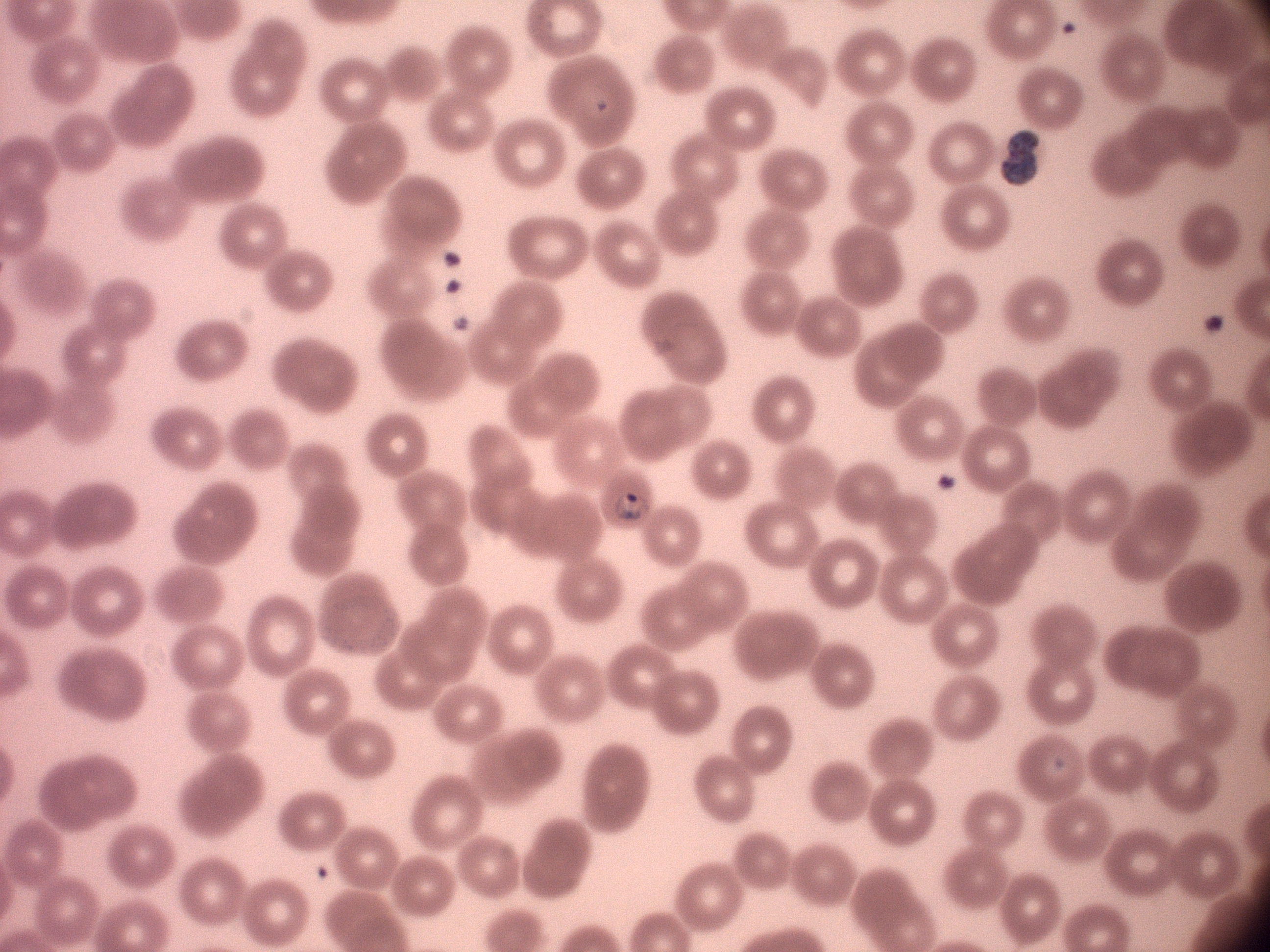
life-cycle stages among the annotated parasites = ring form, trophozoite
magnification = 100x
image size = 1270×952 pixels
species = Plasmodium malariae
preparation = thin blood smear
stain = Giemsa
malaria parasite locations = approximate bounding boxes as (x1, y1, x2, y2) in pixels, from the source annotation, which is not necessarily exhaustive: (1000, 131, 1039, 186), (614, 492, 652, 522)
field of view = one from this slide
microscope = Leica DM2000 with built-in camera